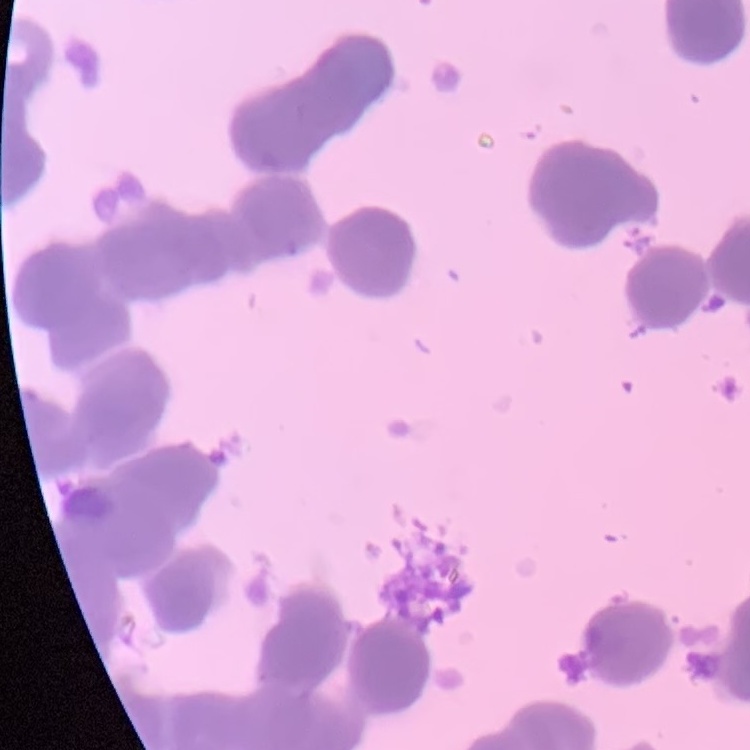
The erythrocytes show rouleaux formation. Thin peripheral smear. Square crop of a larger photomicrograph. Stained with either Field's or Giemsa.